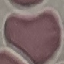

{
  "malaria_status": "uninfected",
  "capture": "smartphone camera at the microscope eyepiece",
  "image_type": "automatically extracted cell patch, resized to 64 × 64 pixels",
  "stain": "Giemsa",
  "preparation": "thin blood smear"
}